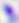
Toxoplasma gondii is shown. Micrograph. Captured at 400x magnification.